Locate every blood parasite and identify its species.
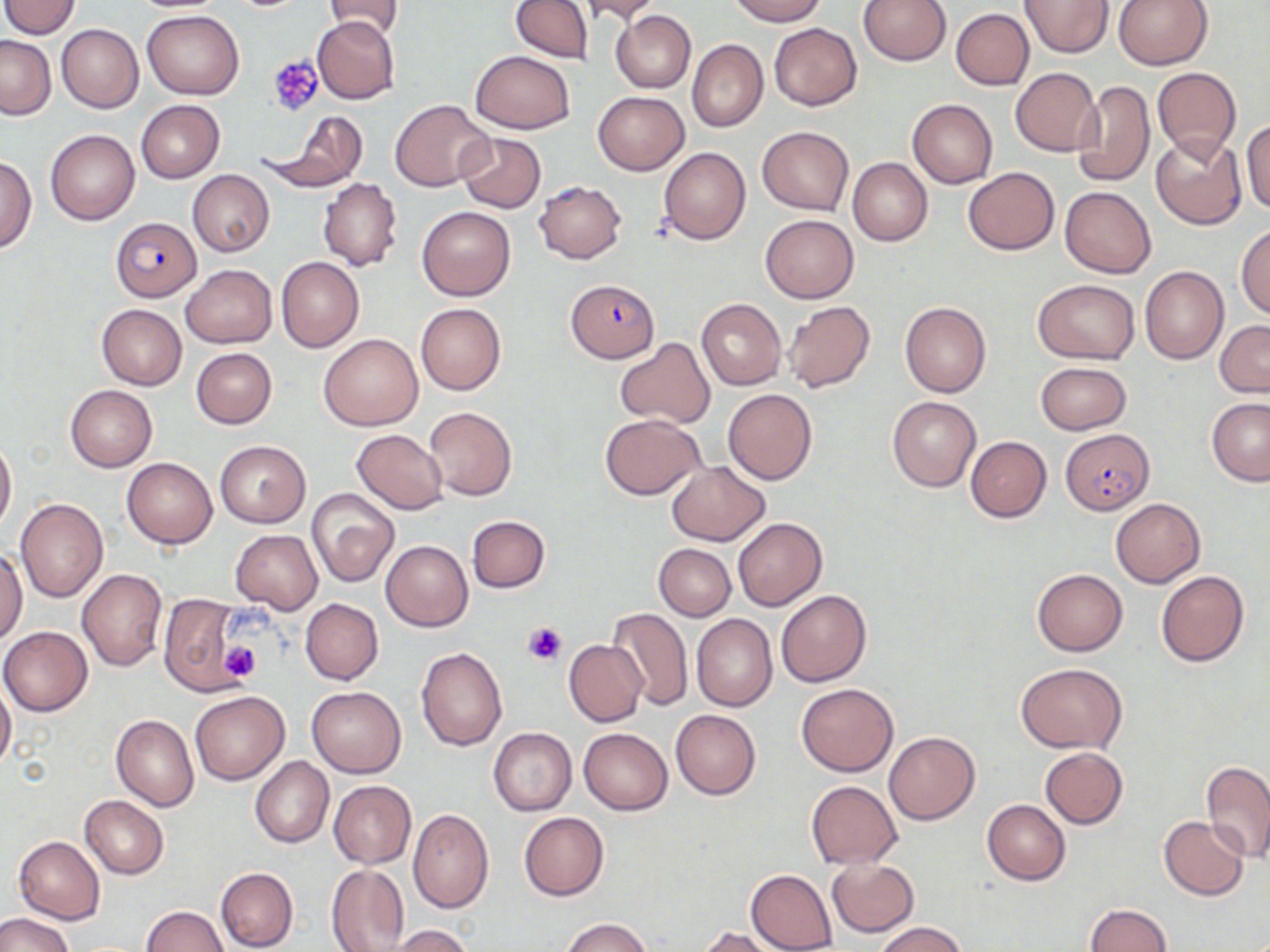

Approximate bounding boxes as named x1/y1/x2/y2 corners in pixels.
Plasmodium falciparum-infected red blood cells: (x1=109, y1=217, x2=203, y2=301), (x1=567, y1=278, x2=659, y2=361), (x1=1060, y1=429, x2=1154, y2=514).
No Plasmodium ovale, Plasmodium malariae, Plasmodium vivax, Babesia divergens, or Trypanosoma brucei observed.

Summary:
  - Uninfected red blood cell locations: (x1=509, y1=0, x2=591, y2=63), (x1=577, y1=0, x2=665, y2=23), (x1=730, y1=0, x2=825, y2=25), (x1=859, y1=0, x2=951, y2=66), (x1=1021, y1=0, x2=1114, y2=57), (x1=1114, y1=0, x2=1213, y2=71), (x1=2, y1=1, x2=80, y2=37), (x1=325, y1=1, x2=403, y2=38), (x1=950, y1=8, x2=1033, y2=90), (x1=142, y1=11, x2=244, y2=98), (x1=611, y1=11, x2=695, y2=93), (x1=312, y1=16, x2=400, y2=103), (x1=57, y1=23, x2=143, y2=113), (x1=769, y1=23, x2=861, y2=110), (x1=1, y1=35, x2=56, y2=119), (x1=686, y1=39, x2=767, y2=131), (x1=471, y1=50, x2=574, y2=134), (x1=1010, y1=67, x2=1101, y2=155), (x1=1152, y1=67, x2=1240, y2=159), (x1=1073, y1=80, x2=1155, y2=188), (x1=592, y1=90, x2=689, y2=175), (x1=389, y1=99, x2=494, y2=192), (x1=908, y1=99, x2=997, y2=187), (x1=135, y1=100, x2=224, y2=182), (x1=266, y1=109, x2=369, y2=191), (x1=1242, y1=120, x2=1270, y2=215), (x1=758, y1=127, x2=853, y2=215), (x1=45, y1=129, x2=139, y2=225), (x1=458, y1=132, x2=546, y2=213), (x1=1150, y1=132, x2=1248, y2=230), (x1=658, y1=146, x2=750, y2=244), (x1=0, y1=154, x2=36, y2=253), (x1=848, y1=158, x2=933, y2=246), (x1=963, y1=167, x2=1059, y2=255), (x1=188, y1=169, x2=274, y2=256), (x1=319, y1=177, x2=402, y2=271), (x1=534, y1=181, x2=626, y2=263), (x1=1059, y1=186, x2=1156, y2=278), (x1=417, y1=206, x2=514, y2=301), (x1=761, y1=214, x2=858, y2=302), (x1=1236, y1=223, x2=1270, y2=320), (x1=276, y1=257, x2=363, y2=352), (x1=179, y1=264, x2=277, y2=349), (x1=1140, y1=266, x2=1228, y2=364), (x1=1034, y1=280, x2=1139, y2=363), (x1=696, y1=298, x2=786, y2=390), (x1=783, y1=301, x2=876, y2=393), (x1=900, y1=301, x2=991, y2=398), (x1=415, y1=303, x2=506, y2=394), (x1=96, y1=304, x2=187, y2=389), (x1=1214, y1=320, x2=1270, y2=397), (x1=319, y1=333, x2=423, y2=431), (x1=614, y1=339, x2=715, y2=427), (x1=191, y1=348, x2=276, y2=429), (x1=1036, y1=361, x2=1130, y2=435), (x1=65, y1=385, x2=157, y2=471), (x1=723, y1=388, x2=817, y2=484), (x1=887, y1=397, x2=980, y2=491), (x1=1207, y1=398, x2=1270, y2=485), (x1=423, y1=406, x2=517, y2=502), (x1=600, y1=414, x2=705, y2=499), (x1=351, y1=429, x2=449, y2=514), (x1=0, y1=435, x2=16, y2=535), (x1=965, y1=435, x2=1051, y2=522), (x1=215, y1=440, x2=310, y2=527), (x1=124, y1=453, x2=309, y2=538), (x1=122, y1=458, x2=217, y2=548), (x1=667, y1=461, x2=770, y2=546), (x1=307, y1=487, x2=400, y2=586), (x1=1111, y1=497, x2=1205, y2=587), (x1=16, y1=498, x2=108, y2=602), (x1=467, y1=515, x2=550, y2=593), (x1=734, y1=518, x2=827, y2=611), (x1=230, y1=529, x2=323, y2=615), (x1=380, y1=540, x2=473, y2=631), (x1=654, y1=544, x2=736, y2=621), (x1=0, y1=547, x2=27, y2=645), (x1=77, y1=569, x2=168, y2=672), (x1=1032, y1=569, x2=1127, y2=656), (x1=1156, y1=570, x2=1249, y2=666), (x1=776, y1=589, x2=872, y2=687), (x1=159, y1=594, x2=245, y2=696), (x1=300, y1=598, x2=383, y2=684), (x1=605, y1=607, x2=692, y2=711), (x1=692, y1=614, x2=777, y2=712), (x1=1, y1=625, x2=92, y2=715), (x1=564, y1=639, x2=646, y2=726), (x1=416, y1=646, x2=507, y2=750), (x1=1015, y1=662, x2=1127, y2=755), (x1=0, y1=680, x2=15, y2=773), (x1=796, y1=683, x2=897, y2=776), (x1=306, y1=686, x2=406, y2=779), (x1=190, y1=691, x2=290, y2=785), (x1=670, y1=709, x2=762, y2=800), (x1=111, y1=715, x2=199, y2=812), (x1=489, y1=727, x2=576, y2=816), (x1=579, y1=727, x2=673, y2=815), (x1=883, y1=731, x2=979, y2=825), (x1=1039, y1=747, x2=1128, y2=829), (x1=250, y1=755, x2=334, y2=848), (x1=1202, y1=761, x2=1270, y2=863), (x1=327, y1=780, x2=416, y2=869), (x1=806, y1=781, x2=902, y2=868), (x1=79, y1=796, x2=168, y2=879), (x1=982, y1=799, x2=1070, y2=885), (x1=408, y1=810, x2=494, y2=914), (x1=519, y1=812, x2=609, y2=900), (x1=1158, y1=816, x2=1250, y2=899), (x1=14, y1=836, x2=105, y2=925), (x1=826, y1=858, x2=919, y2=937), (x1=325, y1=863, x2=409, y2=951), (x1=216, y1=867, x2=298, y2=951), (x1=746, y1=869, x2=837, y2=951), (x1=1083, y1=903, x2=1172, y2=952), (x1=140, y1=906, x2=229, y2=951), (x1=0, y1=911, x2=75, y2=952), (x1=561, y1=917, x2=650, y2=952), (x1=875, y1=922, x2=967, y2=952), (x1=387, y1=925, x2=472, y2=952), (x1=699, y1=926, x2=778, y2=952)
  - Platelet locations: (x1=268, y1=56, x2=323, y2=116), (x1=522, y1=619, x2=569, y2=665), (x1=219, y1=642, x2=262, y2=684)
  - Slide-level diagnosis: Plasmodium falciparum
  - Magnification: 1000x
  - Modality: optical microscopy
  - Image size: 1270×952 pixels
  - Stain: May-Grünwald-Giemsa
  - Preparation: thin blood smear
  - Field of view: one of a larger specimen